Comment on the morphology of the red blood cells.
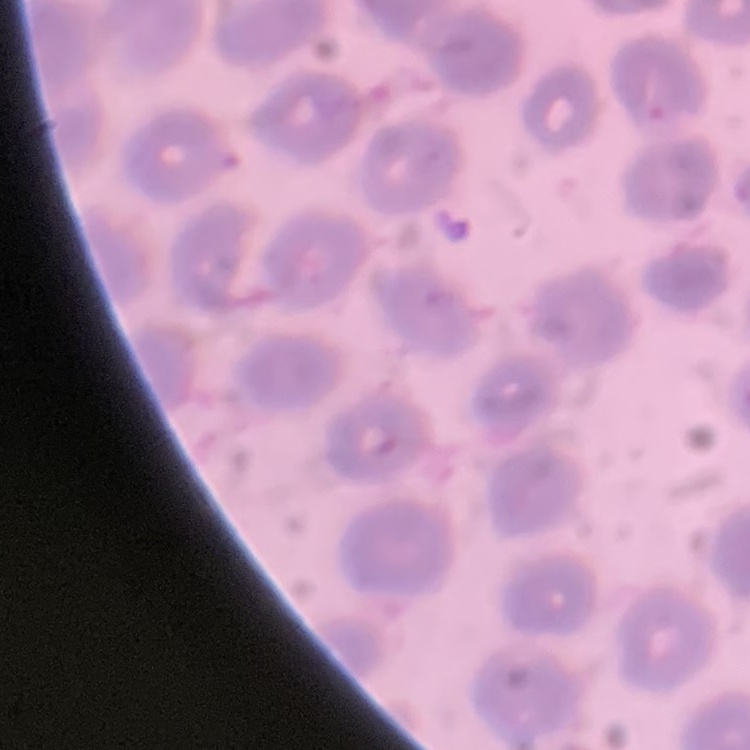
No rouleaux formation.

Summary:
  - Preparation: thin blood smear
  - Stain: Field's or Giemsa
  - Image type: one tile cut from a larger photomicrograph